Assess this cell for malaria.
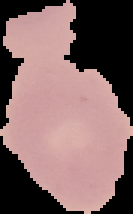

Uninfected.

Summary:
  - Image type: segmented cell region on a black background
  - Image size: 133×214 pixels
  - Preparation: thin blood smear